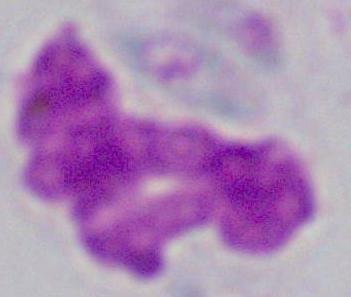
Photomicrograph. Captured at 1000x magnification. A white blood cell is seen.